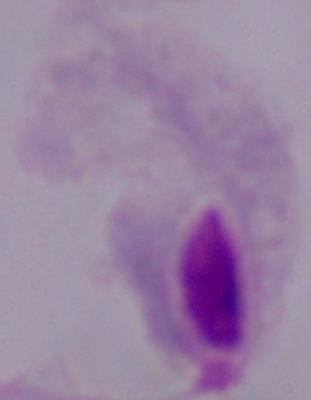
Summary:
  - Modality: micrograph
  - Magnification: 1000x
  - Identification: trichomonad